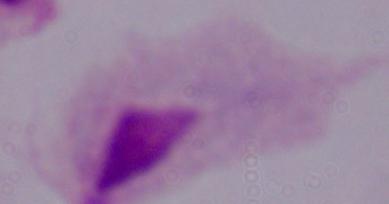

Photomicrograph. Captured at 1000x magnification. A trichomonad is shown.